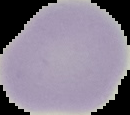
Summary:
  - Image size: 130×115 pixels
  - Malaria status: uninfected
  - Image type: segmented cell region on a black background
  - Preparation: thin blood film